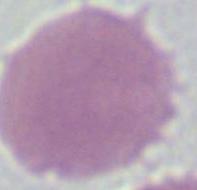

Photomicrograph. 1000x magnification. A red blood cell is seen.